Report the malaria status of this cell.
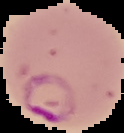
It is parasitized.

image_size: 124×133 pixels
image_type: segmented cell region with the area outside set to black
preparation: thin blood smear